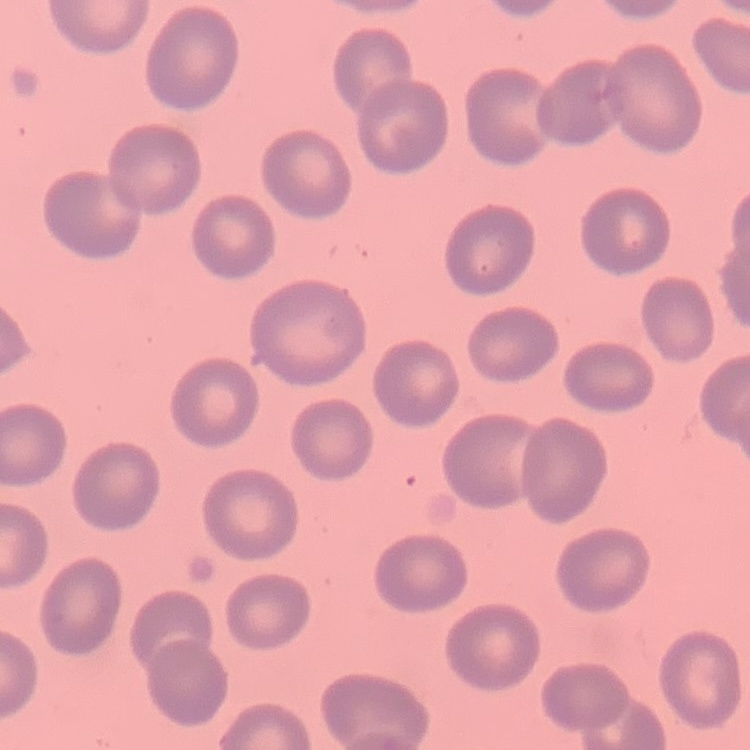

red blood cell morphology = no rouleaux formation
image type = one tile cut from a larger photomicrograph
stain = Field's or Giemsa
preparation = thin blood film